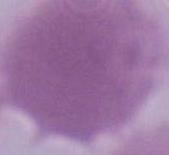
Summary:
  - Identification: erythrocyte
  - Modality: micrograph
  - Magnification: 1000x